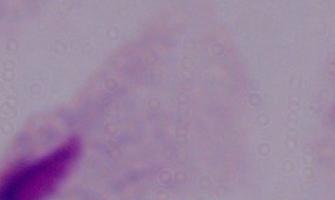

Summary:
  - Magnification: 1000x
  - Modality: photomicrograph
  - Identification: trichomonad